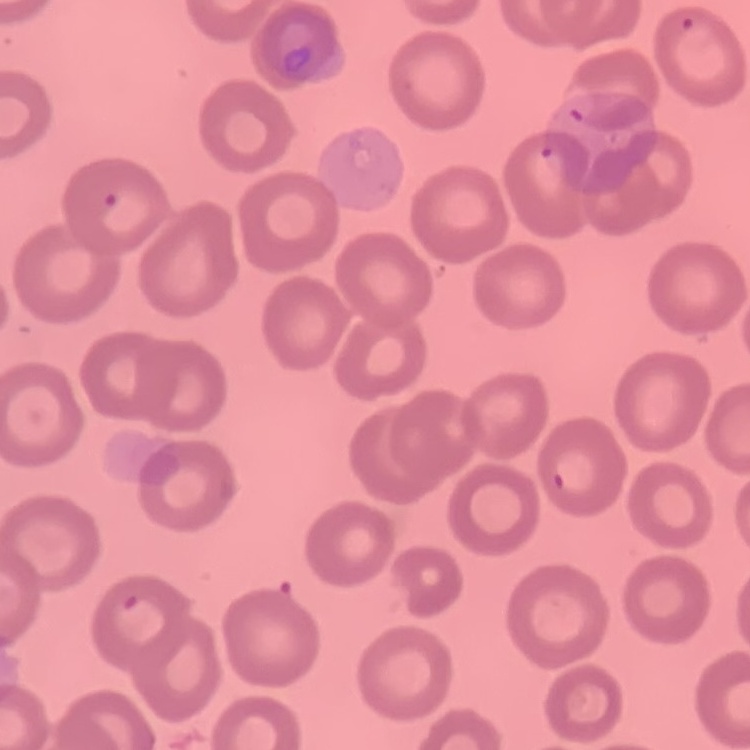
The red blood cells exhibit no rouleaux formation. Square crop of a larger photomicrograph. Thin peripheral smear. Field's or Giemsa stain.